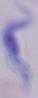
identification = trypanosome
magnification = 1000x
modality = photomicrograph